Report the malaria status of this cell.
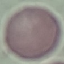
It is uninfected.

Thin blood smear. Automatically extracted cell patch, resized to 64 × 64 pixels. Photographed with a smartphone camera at the microscope eyepiece. Giemsa-stained preparation.